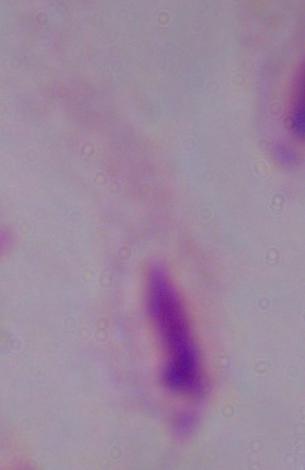

identification = trichomonad
modality = photomicrograph
magnification = 1000x